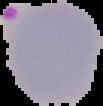

From a thin blood film. Image is 103×106 pixels. Cell region segmented out of the field of view; the surrounding area is masked to black. Malaria status: parasitized.